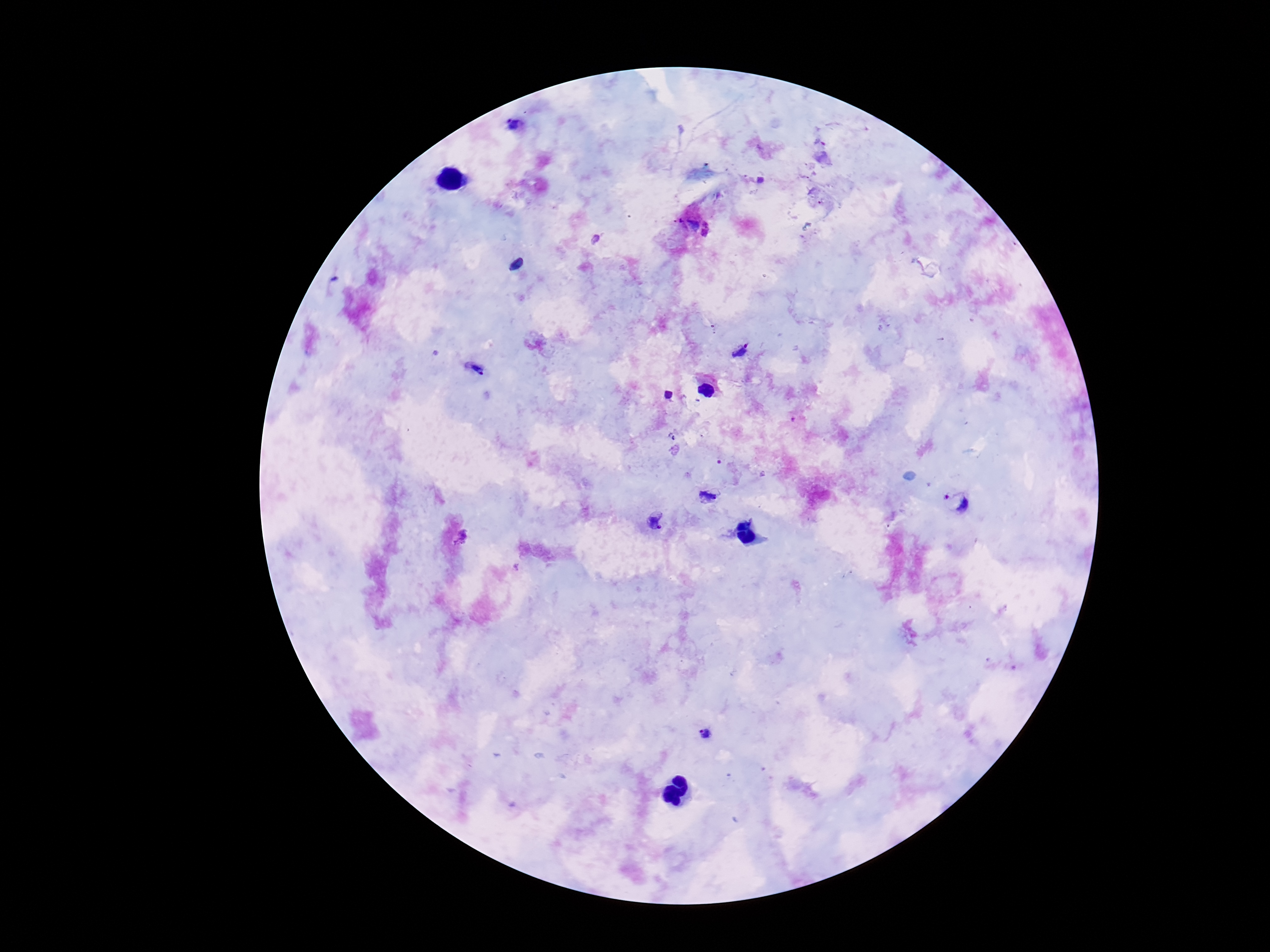
field of view = one from this slide
image size = 1270×952 pixels
magnification = 100x
capture = smartphone camera through the microscope eyepiece
Plasmodium parasite locations = approximate centers as {x, y} in pixels: {518, 128}, {822, 153}, {740, 351}, {475, 368}, {710, 495}, {957, 502}, {654, 520}, {462, 538}, {707, 733}
stain = Giemsa
preparation = thick blood smear
patient malaria status = positive